Report the malaria status of this cell.
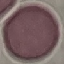

It is uninfected.

capture: smartphone camera at the microscope eyepiece
image_type: automatically extracted cell patch, resized to 64 × 64 pixels
stain: Giemsa
preparation: thin blood smear